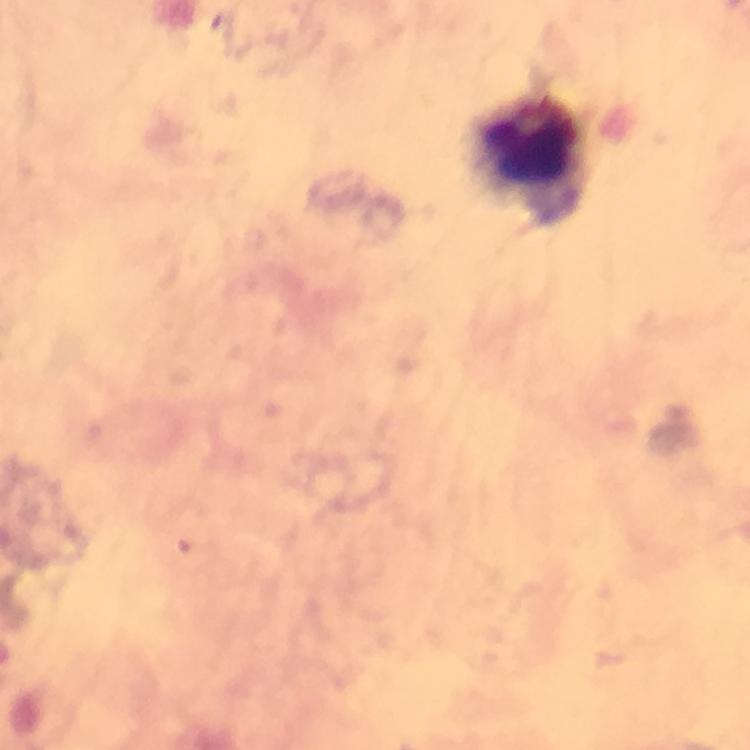
Approximate centers as [x, y] in pixels.
Summary:
  - Leukocyte locations: [526, 157]
  - Cropped from: one field of view
  - Magnification: 100x
  - Capture: smartphone mounted on the microscope
  - Immersion oil: used
  - Preparation: thick smear
  - Image size: 750×750 pixels
  - Malaria parasites: none detected
  - Stain: Giemsa
  - Context: from a malaria diagnostic workup